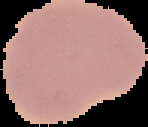
{
  "image_type": "segmented cell region with the area outside set to black",
  "result": "negative for Plasmodium parasites",
  "preparation": "thin blood film",
  "image_size": "148×127 pixels"
}